Name the cell type shown.
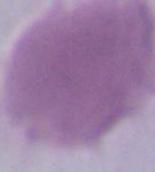

This is an erythrocyte.

Summary:
  - Magnification: 1000x
  - Modality: photomicrograph